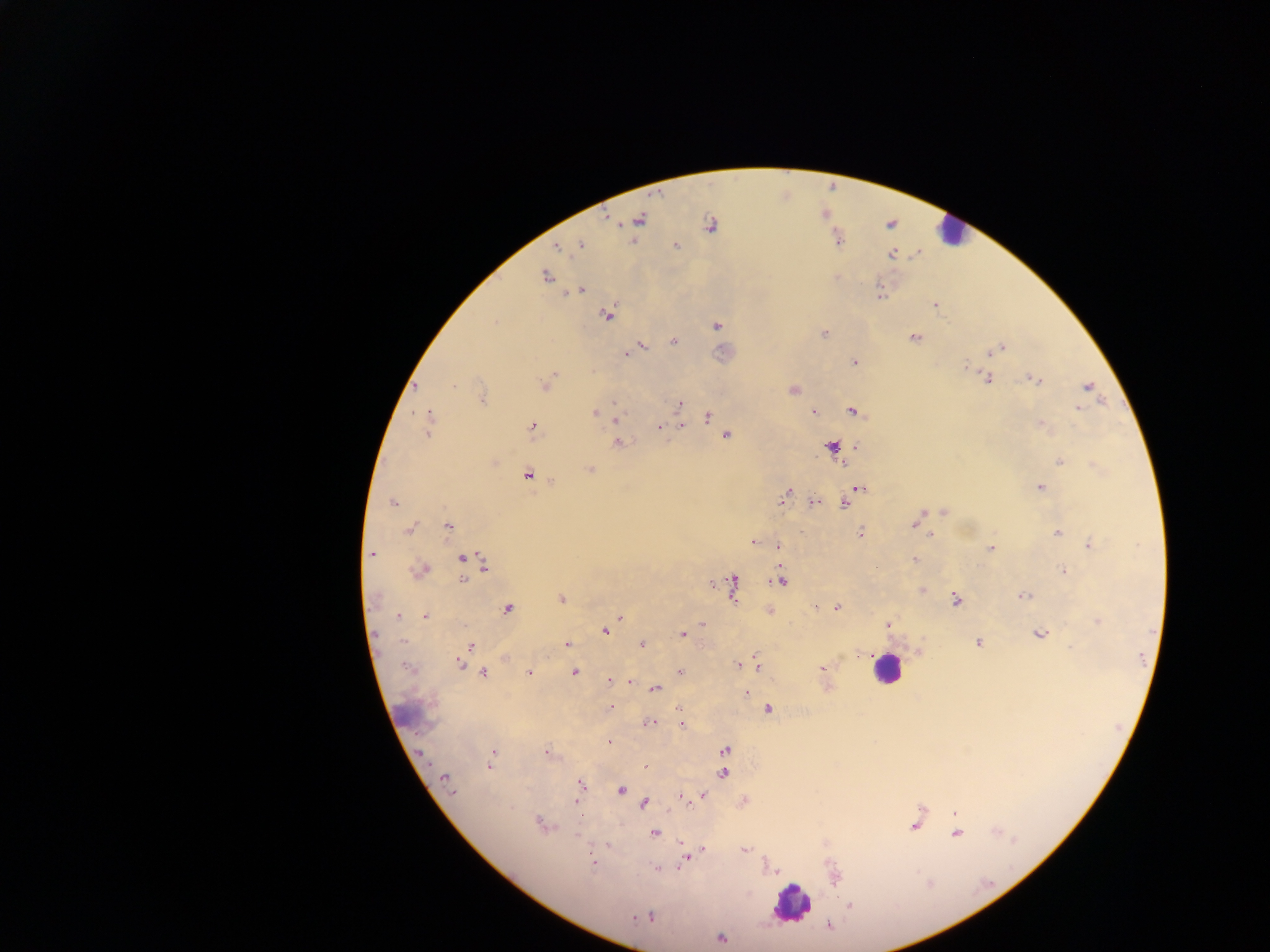

Approximate centers as [x, y] in pixels.
Summary:
  - Malaria parasite locations: [639, 219], [709, 224], [581, 245], [676, 246], [559, 249], [545, 276], [583, 289], [604, 314], [495, 323], [717, 325], [823, 333], [915, 338], [673, 342], [643, 346], [1003, 347], [623, 354], [852, 361], [964, 365], [988, 378], [1030, 378], [1038, 379], [546, 382], [453, 383], [1086, 386], [793, 390], [614, 401], [679, 403], [1078, 409], [851, 410], [813, 411], [594, 412], [430, 414], [707, 417], [615, 419], [1039, 425], [660, 426], [531, 427], [726, 434], [428, 436], [618, 440], [832, 447], [1060, 462], [591, 470], [528, 474], [552, 480], [1040, 486], [859, 488], [789, 489], [786, 492], [782, 500], [812, 502], [392, 503], [844, 503], [941, 512], [922, 515], [914, 523], [408, 527], [448, 528], [861, 532], [1055, 532], [934, 533], [932, 534], [753, 543], [1088, 543], [779, 545], [991, 549], [371, 553], [914, 559], [461, 560], [482, 563], [419, 569], [1062, 570], [780, 580], [463, 581], [709, 583], [733, 588], [922, 589], [1020, 597], [376, 598], [562, 598], [956, 598], [814, 606], [836, 607], [508, 609], [424, 615], [399, 616], [621, 617], [1098, 622], [702, 623], [607, 630], [1037, 633], [682, 634], [402, 639], [977, 642], [564, 644], [641, 644], [471, 646], [1067, 646], [505, 659], [459, 662], [737, 663], [757, 666], [821, 668], [576, 671], [678, 671], [483, 672], [529, 672], [609, 681], [629, 681], [656, 689], [746, 693], [611, 707], [767, 709], [679, 710], [649, 722], [682, 725], [608, 741], [547, 749], [725, 750], [543, 751], [422, 754], [489, 766], [645, 766], [724, 773], [445, 776], [581, 782], [622, 790], [451, 791], [678, 795], [703, 795], [575, 803], [645, 804], [687, 804], [956, 814], [539, 821], [914, 826], [655, 833], [569, 834], [957, 835], [580, 838], [606, 843], [703, 849], [743, 849], [682, 861], [593, 862], [678, 867], [657, 868], [849, 905], [720, 938]
  - Leukocyte locations: [947, 237], [886, 671], [793, 903]
  - Preparation: thick blood film
  - Capture: mobile-phone photograph through a microscope
  - Image size: 1270×952 pixels
  - Field of view: single
  - Country: Ghana